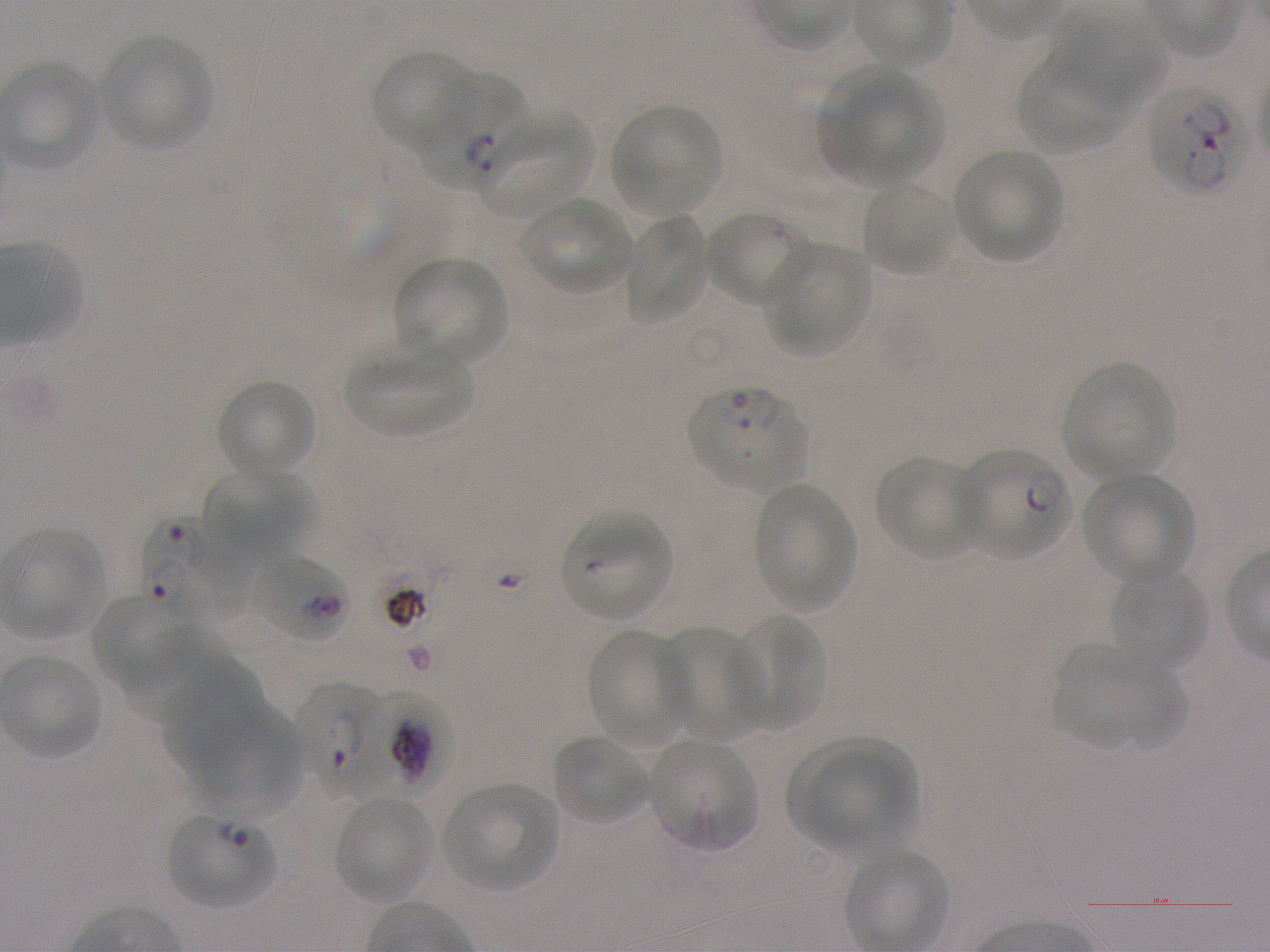 Approximate bounding boxes as {x1, y1, x2, y2} in pixels. Not every red blood cell is marked. A life-cycle stage — or a range of stages, where the recorded stages span more than one — follows each staged infected red blood cell. Locations of red blood cells of indeterminate infection status: {250, 551, 351, 644}. Locations of uninfected red blood cells: {1052, 11, 1170, 116}, {98, 34, 213, 151}, {372, 50, 476, 152}, {1017, 61, 1128, 156}, {824, 69, 941, 185}, {609, 104, 724, 215}, {485, 112, 594, 216}, {953, 147, 1066, 262}, {861, 181, 957, 277}, {521, 197, 634, 295}, {705, 209, 812, 307}, {623, 214, 710, 325}, {766, 243, 873, 357}, {395, 256, 509, 366}, {346, 343, 476, 439}, {1061, 361, 1177, 478}, {216, 378, 318, 479}, {873, 455, 986, 560}, {202, 469, 311, 556}, {1081, 471, 1195, 582}, {753, 480, 857, 612}, {560, 510, 673, 620}, {6, 528, 108, 638}, {1113, 567, 1207, 672}, {91, 593, 187, 690}, {728, 614, 826, 732}, {657, 623, 765, 740}, {118, 624, 221, 719}, {586, 629, 691, 748}, {1052, 646, 1149, 750}, {162, 663, 262, 783}, {1107, 665, 1188, 752}, {199, 704, 307, 817}, {551, 733, 649, 826}, {647, 738, 759, 853}, {785, 738, 916, 839}, {809, 749, 915, 851}, {443, 782, 558, 891}, {335, 796, 435, 903}. Locations of infected red blood cells: {416, 76, 532, 188} ring; {1145, 85, 1244, 194}; {687, 384, 808, 491} ring; {957, 446, 1072, 560} ring; {143, 519, 240, 622}; {308, 684, 376, 798} early ring to early trophozoite; {369, 685, 449, 804}; {168, 812, 277, 910} ring. Image is 1270×952 pixels. One field from this slide. Donor blood group A+. 100x objective under oil immersion, numerical aperture 1.25. P. falciparum strain NF54 maintained in static in-vitro culture. Giemsa stain. Thin blood smear.